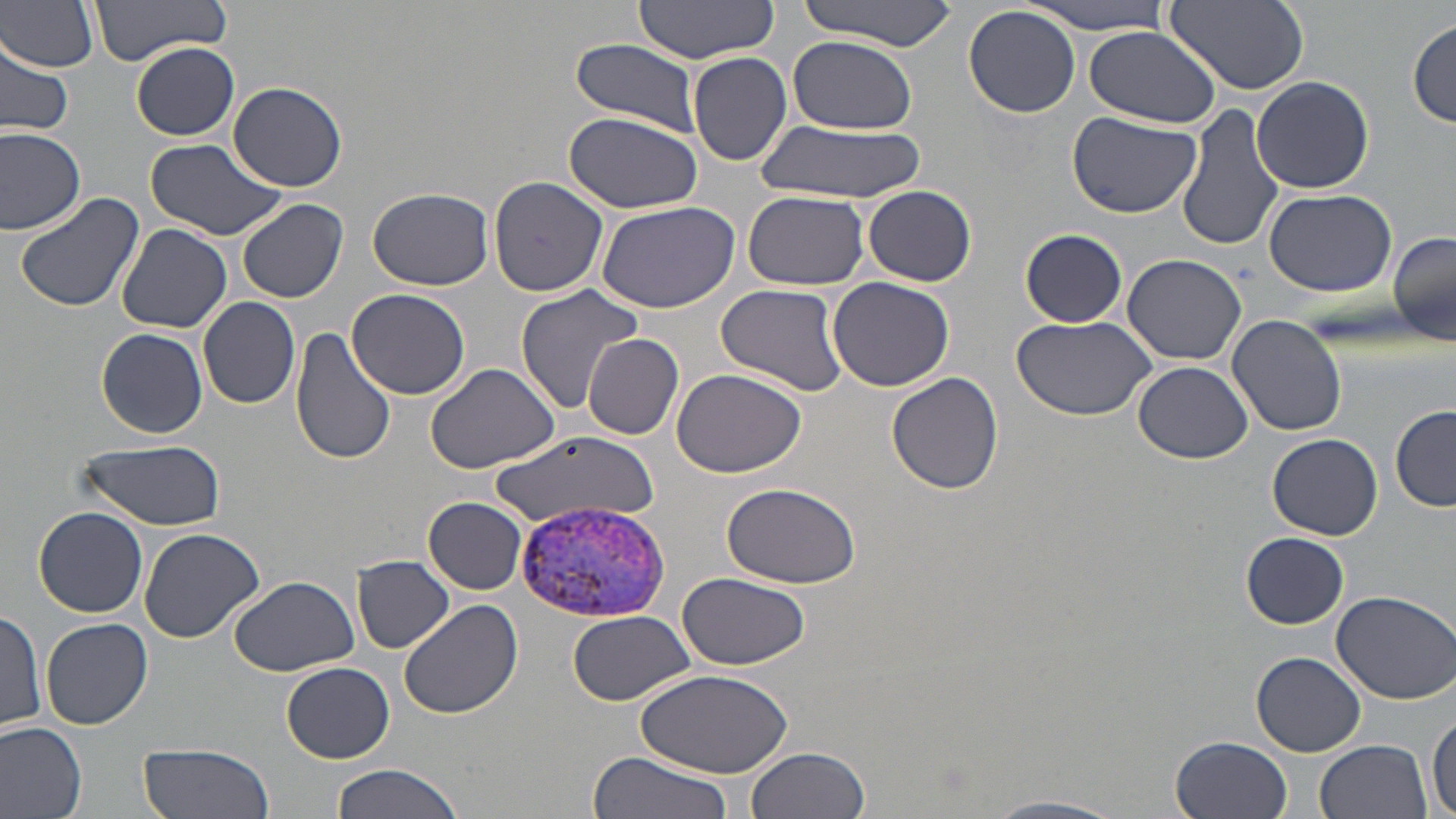
Approximate bounding boxes as [x1, y1, x2, y2] in pixels. Plasmodium vivax-infected red blood cell locations: [513, 501, 674, 624]. Uninfected red blood cell locations: [2, 0, 101, 72], [90, 0, 234, 61], [1026, 0, 1175, 32], [632, 1, 779, 62], [797, 1, 958, 50], [1165, 2, 1309, 94], [964, 7, 1081, 119], [1409, 18, 1456, 127], [1082, 24, 1224, 128], [787, 36, 917, 132], [571, 39, 703, 135], [0, 41, 72, 138], [132, 42, 239, 140], [687, 51, 793, 166], [1251, 75, 1374, 193], [227, 81, 348, 193], [166, 101, 335, 223], [1177, 103, 1284, 254], [1066, 109, 1203, 219], [563, 110, 703, 212], [755, 121, 921, 204], [0, 124, 86, 235], [145, 138, 289, 240], [488, 176, 611, 298], [861, 185, 976, 285], [368, 186, 495, 291], [1264, 187, 1396, 297], [13, 190, 147, 314], [742, 190, 868, 290], [237, 198, 348, 303], [596, 200, 741, 313], [117, 223, 233, 332], [1020, 228, 1127, 327], [1388, 230, 1455, 345], [1123, 253, 1249, 364], [827, 276, 956, 391], [716, 283, 849, 395], [514, 284, 645, 413], [348, 289, 471, 401], [198, 296, 301, 409], [1008, 314, 1157, 420], [1227, 316, 1348, 436], [96, 328, 207, 438], [290, 328, 397, 467], [582, 333, 684, 440], [425, 362, 561, 475], [1132, 363, 1254, 464], [671, 367, 806, 479], [886, 372, 1005, 495], [1391, 403, 1456, 512], [491, 433, 666, 531], [1267, 434, 1383, 540], [74, 439, 227, 530], [720, 480, 865, 586], [424, 497, 528, 595], [34, 506, 148, 617], [138, 527, 264, 642], [1241, 532, 1349, 628], [352, 554, 455, 655], [674, 572, 811, 669], [227, 576, 360, 675], [1329, 590, 1456, 704], [399, 597, 524, 719], [0, 608, 48, 733], [567, 609, 695, 705], [42, 617, 153, 729], [1251, 651, 1366, 757], [281, 661, 394, 762], [631, 666, 794, 777], [1428, 708, 1456, 817], [0, 719, 87, 819], [1172, 734, 1294, 819], [137, 739, 274, 819], [1316, 739, 1433, 819], [744, 747, 870, 819], [584, 752, 736, 819], [329, 764, 468, 819], [982, 795, 1128, 819]. Slide-level diagnosis: Plasmodium vivax. Thin blood smear. Optical microscopy. Image is 1456×819 pixels. 1000x magnification. May-Grünwald-Giemsa-stained preparation. One field of a larger specimen.